Classify this cell by malaria status.
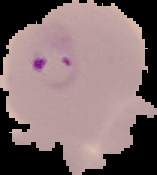
It is parasitized.

From a thin blood film. Image is 157×175 pixels. The area outside the segmented cell region is set to black.